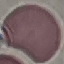
malaria status = uninfected
stain = Giemsa
image type = automatically extracted cell patch, resized to 64 × 64 pixels
preparation = thin blood film
capture = smartphone camera at the microscope eyepiece